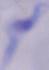
{
  "magnification": "1000x",
  "identification": "trypanosome",
  "modality": "photomicrograph"
}